Identify the parasite.
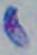
Toxoplasma gondii.

Summary:
  - Magnification: 1000x
  - Modality: micrograph